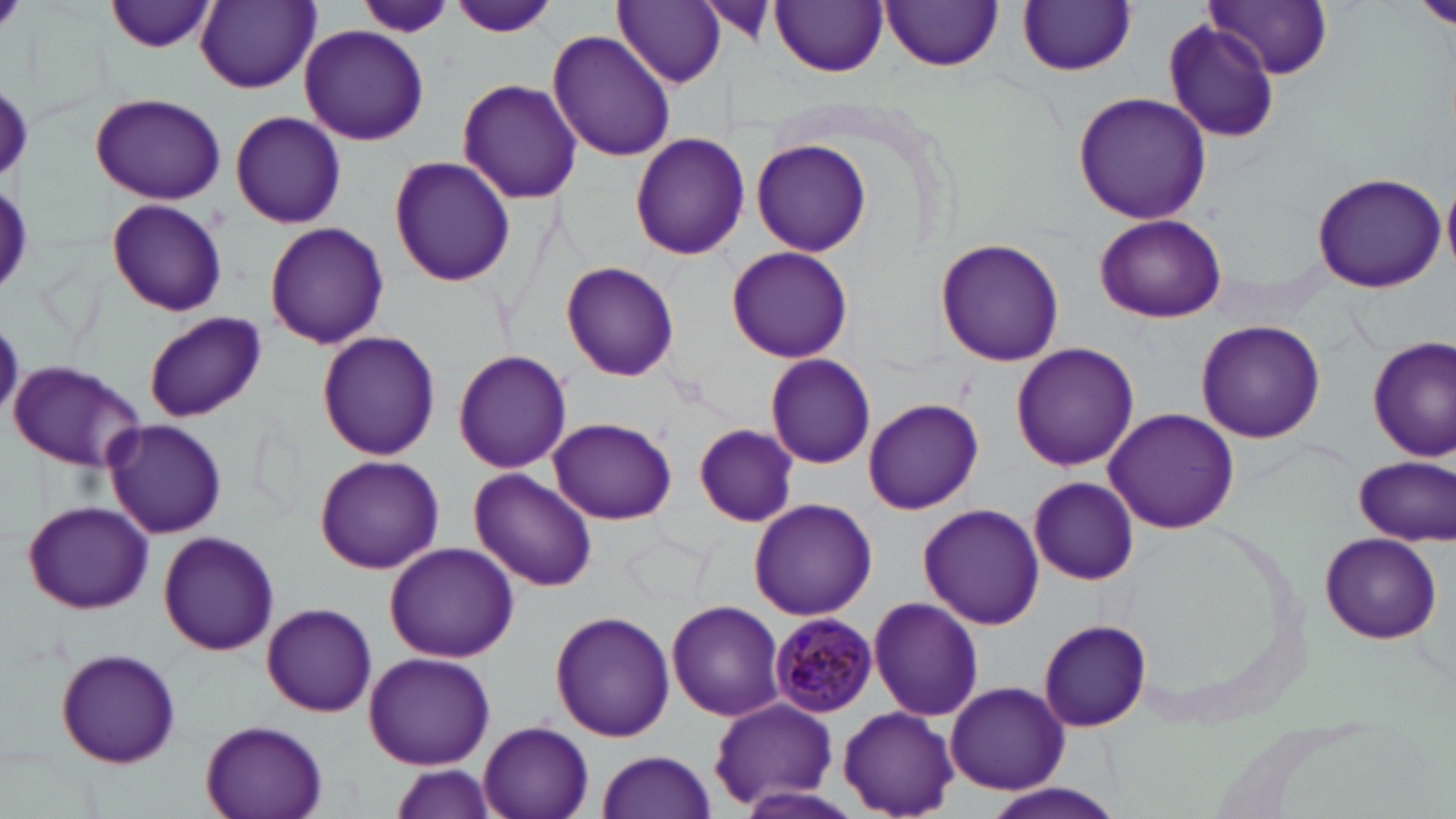
slide_level_diagnosis: Plasmodium malariae
preparation: thin blood film
plasmodium_malariae_infected_red_blood_cell_locations: 'approximate bounding boxes as [x1, y1, x2, y2] in pixels: [769, 612, 880, 719]'
uninfected_red_blood_cell_locations: 'approximate bounding boxes as [x1, y1, x2, y2] in pixels: [106, 0, 217, 52], [613, 0, 728, 88], [695, 0, 779, 47], [1204, 0, 1333, 80], [194, 1, 319, 94], [358, 1, 454, 40], [771, 1, 888, 76], [882, 1, 1002, 72], [449, 2, 559, 40], [1020, 2, 1135, 76], [1163, 22, 1283, 142], [299, 25, 430, 147], [548, 28, 676, 161], [456, 79, 583, 206], [1072, 92, 1211, 224], [89, 93, 225, 205], [229, 109, 346, 230], [630, 132, 749, 258], [752, 138, 873, 256], [388, 155, 516, 286], [1311, 171, 1446, 292], [1442, 176, 1456, 273], [106, 197, 228, 317], [1095, 213, 1226, 322], [264, 222, 389, 350], [936, 239, 1063, 366], [727, 246, 853, 362], [562, 262, 679, 382], [144, 312, 265, 422], [1196, 320, 1326, 444], [316, 331, 441, 461], [1368, 335, 1456, 461], [1011, 342, 1139, 470], [453, 349, 572, 473], [766, 354, 876, 470], [7, 360, 147, 473], [862, 397, 983, 513], [1104, 407, 1241, 534], [549, 417, 676, 524], [102, 418, 228, 538], [693, 424, 799, 527], [314, 455, 443, 573], [1356, 455, 1453, 544], [470, 469, 597, 591], [1027, 477, 1138, 585], [749, 498, 877, 620], [23, 501, 153, 614], [919, 503, 1043, 629], [157, 532, 281, 656], [1318, 532, 1442, 644], [384, 541, 517, 661], [868, 596, 984, 721], [666, 600, 785, 721], [262, 602, 376, 717], [551, 609, 673, 741], [1039, 619, 1152, 731], [54, 646, 182, 768], [363, 651, 495, 769], [945, 681, 1070, 795], [708, 699, 839, 810], [838, 706, 959, 817], [1205, 706, 1383, 815], [198, 718, 330, 819], [477, 720, 595, 819], [596, 751, 717, 819], [387, 763, 500, 819], [976, 780, 1128, 819], [732, 786, 864, 819]'
image_size: 1456×819 pixels
stain: May-Grünwald-Giemsa
modality: optical microscopy
magnification: 1000x
field_of_view: one of a larger specimen